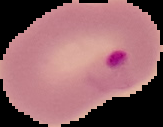
image_type: segmented cell region with the area outside set to black
image_size: 163×127 pixels
malaria_status: parasitized
preparation: thin blood film